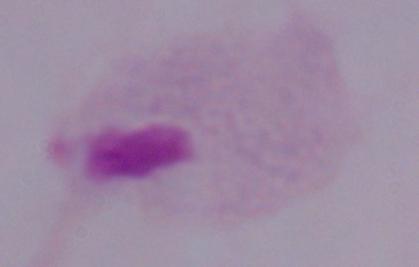
Summary:
  - Identification: trichomonad
  - Magnification: 1000x
  - Modality: micrograph